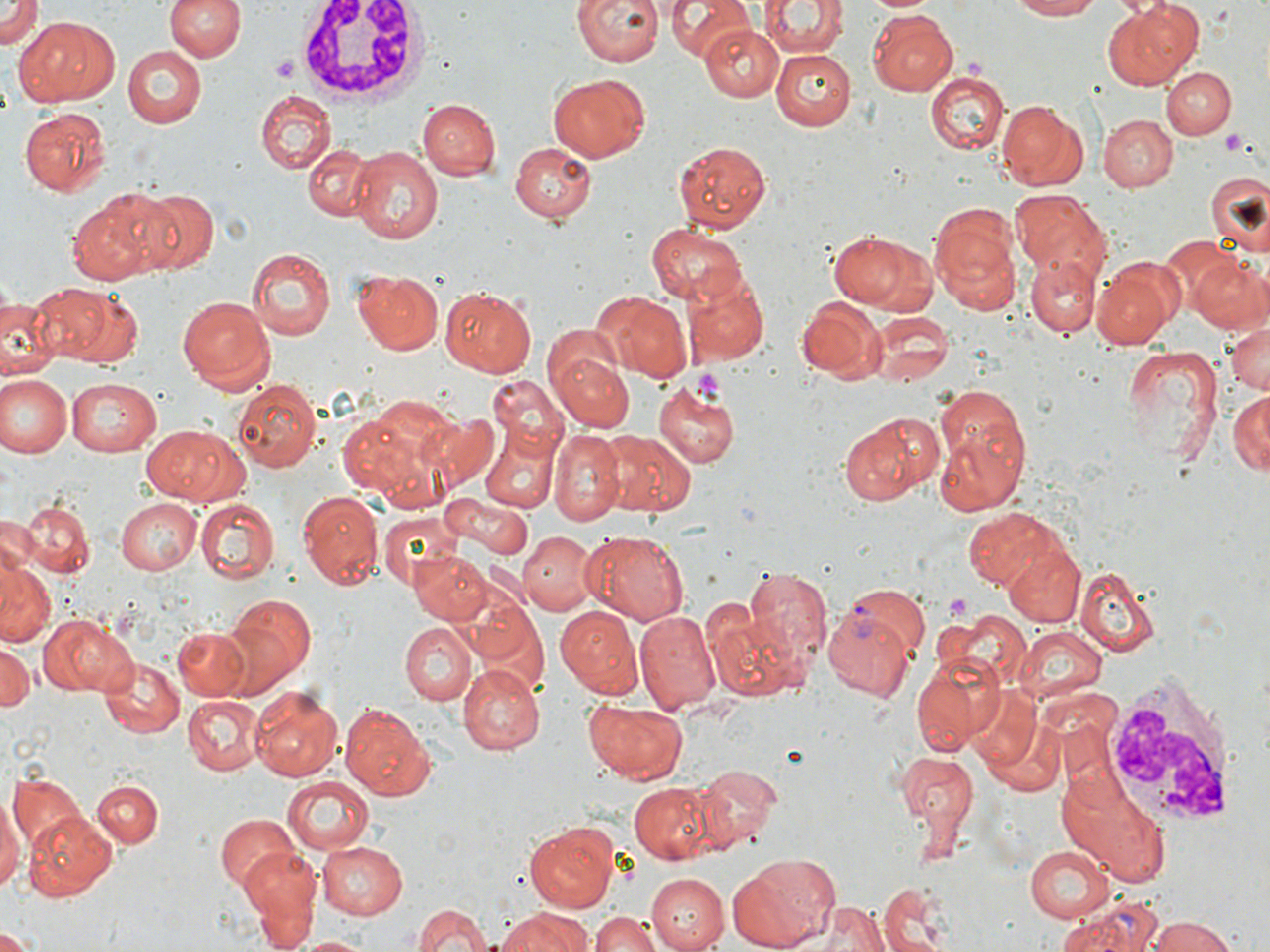

{
  "slide_level_diagnosis": "Plasmodium vivax",
  "image_size": "1270×952 pixels",
  "field_of_view": "single",
  "stain": "May-Grünwald-Giemsa",
  "white_blood_cell_locations": "approximate bounding boxes as named x1/y1/x2/y2 corners in pixels: (x1=296, y1=0, x2=430, y2=107), (x1=1102, y1=670, x2=1243, y2=831)",
  "uninfected_red_blood_cell_locations": "approximate bounding boxes as named x1/y1/x2/y2 corners in pixels: (x1=0, y1=0, x2=41, y2=48), (x1=165, y1=0, x2=243, y2=63), (x1=573, y1=0, x2=663, y2=67), (x1=667, y1=0, x2=754, y2=61), (x1=760, y1=0, x2=846, y2=57), (x1=869, y1=0, x2=934, y2=15), (x1=1007, y1=0, x2=1108, y2=21), (x1=1104, y1=2, x2=1200, y2=89), (x1=866, y1=11, x2=957, y2=97), (x1=21, y1=16, x2=120, y2=104), (x1=702, y1=25, x2=782, y2=104), (x1=122, y1=45, x2=206, y2=126), (x1=773, y1=48, x2=857, y2=130), (x1=1161, y1=66, x2=1235, y2=139), (x1=926, y1=73, x2=1008, y2=155), (x1=546, y1=74, x2=650, y2=162), (x1=255, y1=90, x2=337, y2=173), (x1=995, y1=97, x2=1088, y2=188), (x1=417, y1=98, x2=499, y2=181), (x1=18, y1=107, x2=109, y2=195), (x1=1098, y1=113, x2=1177, y2=191), (x1=670, y1=139, x2=771, y2=232), (x1=508, y1=140, x2=595, y2=223), (x1=302, y1=142, x2=374, y2=222), (x1=348, y1=145, x2=444, y2=244), (x1=1207, y1=171, x2=1269, y2=253), (x1=137, y1=186, x2=220, y2=274), (x1=68, y1=190, x2=170, y2=285), (x1=1011, y1=191, x2=1111, y2=278), (x1=930, y1=206, x2=1023, y2=318), (x1=646, y1=222, x2=747, y2=305), (x1=826, y1=228, x2=939, y2=314), (x1=1158, y1=236, x2=1242, y2=317), (x1=245, y1=246, x2=336, y2=341), (x1=1028, y1=252, x2=1104, y2=337), (x1=1190, y1=256, x2=1270, y2=334), (x1=1091, y1=258, x2=1181, y2=350), (x1=353, y1=267, x2=444, y2=356), (x1=684, y1=275, x2=768, y2=365), (x1=10, y1=283, x2=115, y2=372), (x1=438, y1=283, x2=536, y2=376), (x1=55, y1=285, x2=145, y2=369), (x1=590, y1=289, x2=692, y2=382), (x1=178, y1=294, x2=275, y2=391), (x1=0, y1=296, x2=60, y2=378), (x1=796, y1=297, x2=887, y2=384), (x1=869, y1=309, x2=951, y2=387), (x1=1224, y1=320, x2=1269, y2=399), (x1=1119, y1=344, x2=1226, y2=466), (x1=550, y1=348, x2=636, y2=432), (x1=2, y1=375, x2=71, y2=458), (x1=488, y1=376, x2=570, y2=456), (x1=233, y1=377, x2=320, y2=472), (x1=66, y1=378, x2=163, y2=456), (x1=654, y1=383, x2=739, y2=469), (x1=933, y1=384, x2=1031, y2=485), (x1=1228, y1=391, x2=1269, y2=476), (x1=337, y1=407, x2=438, y2=497), (x1=837, y1=412, x2=938, y2=506), (x1=143, y1=422, x2=246, y2=505), (x1=478, y1=427, x2=558, y2=515), (x1=933, y1=427, x2=1029, y2=516), (x1=550, y1=430, x2=629, y2=524), (x1=601, y1=432, x2=697, y2=516), (x1=297, y1=491, x2=383, y2=589), (x1=14, y1=496, x2=95, y2=582), (x1=445, y1=496, x2=535, y2=559), (x1=114, y1=498, x2=202, y2=575), (x1=196, y1=499, x2=280, y2=584), (x1=961, y1=505, x2=1065, y2=587), (x1=0, y1=510, x2=41, y2=579), (x1=379, y1=512, x2=459, y2=588), (x1=518, y1=531, x2=601, y2=613), (x1=592, y1=531, x2=690, y2=625), (x1=1001, y1=541, x2=1086, y2=629), (x1=410, y1=554, x2=493, y2=625), (x1=0, y1=560, x2=55, y2=644), (x1=741, y1=563, x2=832, y2=664), (x1=1075, y1=564, x2=1164, y2=659), (x1=223, y1=595, x2=317, y2=695), (x1=555, y1=605, x2=642, y2=699), (x1=710, y1=609, x2=803, y2=704), (x1=634, y1=612, x2=720, y2=711), (x1=934, y1=612, x2=1031, y2=690), (x1=41, y1=613, x2=138, y2=695), (x1=400, y1=621, x2=476, y2=703), (x1=1012, y1=625, x2=1106, y2=703), (x1=173, y1=627, x2=252, y2=699), (x1=0, y1=642, x2=36, y2=710), (x1=99, y1=659, x2=185, y2=739), (x1=909, y1=660, x2=997, y2=754), (x1=458, y1=662, x2=544, y2=754), (x1=962, y1=681, x2=1044, y2=773), (x1=250, y1=687, x2=344, y2=781), (x1=185, y1=695, x2=263, y2=775), (x1=581, y1=700, x2=690, y2=782), (x1=336, y1=701, x2=435, y2=800), (x1=893, y1=750, x2=979, y2=845), (x1=697, y1=764, x2=782, y2=847), (x1=1058, y1=772, x2=1175, y2=886), (x1=7, y1=773, x2=86, y2=849), (x1=282, y1=777, x2=374, y2=851), (x1=95, y1=781, x2=162, y2=848), (x1=627, y1=782, x2=725, y2=864), (x1=0, y1=795, x2=22, y2=896), (x1=25, y1=810, x2=118, y2=896), (x1=215, y1=814, x2=301, y2=893), (x1=523, y1=820, x2=620, y2=910), (x1=314, y1=839, x2=407, y2=920), (x1=1024, y1=843, x2=1116, y2=920), (x1=239, y1=849, x2=322, y2=946), (x1=730, y1=853, x2=838, y2=948), (x1=647, y1=872, x2=728, y2=951), (x1=877, y1=882, x2=958, y2=952), (x1=802, y1=898, x2=888, y2=952), (x1=1054, y1=900, x2=1157, y2=952), (x1=408, y1=903, x2=500, y2=952), (x1=498, y1=907, x2=597, y2=951), (x1=591, y1=911, x2=665, y2=952), (x1=1138, y1=915, x2=1242, y2=952), (x1=0, y1=929, x2=35, y2=951), (x1=288, y1=934, x2=375, y2=951)",
  "modality": "light microscopy",
  "preparation": "thin blood smear",
  "platelet_locations": "approximate bounding boxes as named x1/y1/x2/y2 corners in pixels: (x1=273, y1=56, x2=300, y2=82), (x1=1222, y1=129, x2=1248, y2=157), (x1=690, y1=366, x2=727, y2=403), (x1=943, y1=593, x2=973, y2=621)",
  "magnification": "1000x",
  "plasmodium_vivax_infected_red_blood_cell_locations": "approximate bounding boxes as named x1/y1/x2/y2 corners in pixels: (x1=822, y1=596, x2=925, y2=700)"
}